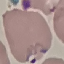
result = malaria parasites identified
capture = smartphone through the microscope eyepiece
stain = Giemsa
image type = cell patch, automatically extracted from a larger field of view and resized to 64 × 64 pixels
preparation = thin blood film